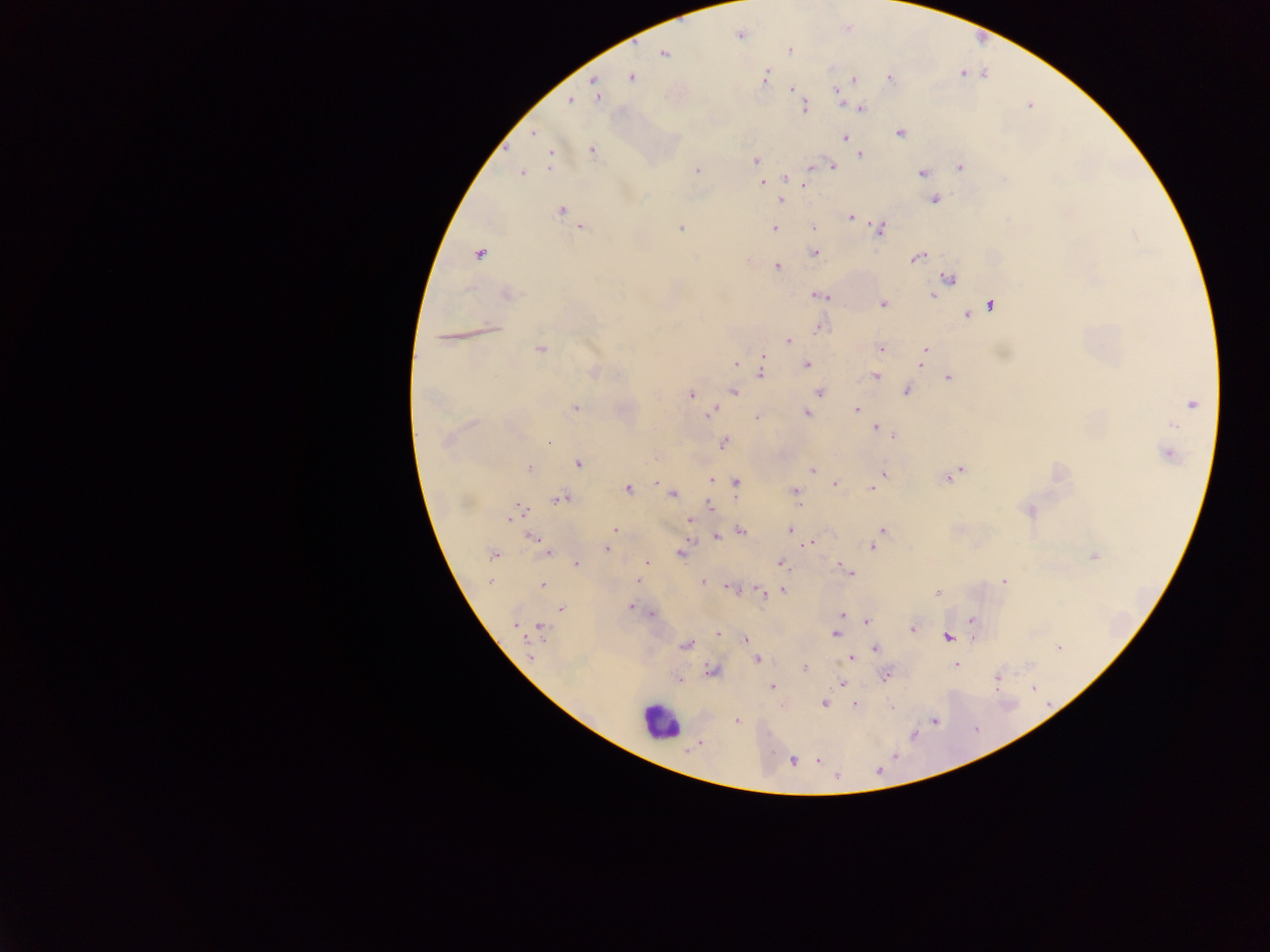
Approximate centers as (x, y) in pixels.
Summary:
  - Leukocyte locations: (658, 722)
  - Plasmodium parasite locations: (741, 35), (789, 50), (664, 53), (631, 77), (765, 77), (890, 78), (854, 80), (594, 81), (792, 89), (837, 92), (597, 95), (569, 101), (804, 107), (860, 108), (534, 133), (901, 133), (844, 137), (592, 150), (861, 155), (550, 158), (755, 160), (831, 166), (960, 167), (697, 170), (522, 172), (922, 173), (785, 178), (762, 183), (806, 185), (781, 200), (934, 200), (561, 211), (850, 216), (813, 227), (581, 228), (680, 228), (774, 229), (879, 229), (815, 253), (479, 254), (918, 257), (777, 267), (949, 278), (937, 287), (507, 294), (933, 294), (820, 295), (883, 304), (990, 305), (967, 315), (820, 327), (444, 338), (787, 341), (541, 349), (881, 349), (925, 350), (923, 356), (763, 359), (736, 363), (921, 364), (807, 365), (760, 371), (593, 372), (876, 375), (949, 378), (735, 391), (906, 391), (820, 392), (691, 394), (1192, 404), (575, 408), (856, 410), (711, 412), (807, 413), (757, 417), (1171, 424), (877, 428), (891, 435), (446, 441), (549, 442), (723, 443), (1168, 454), (578, 464), (529, 468), (812, 469), (960, 471), (884, 475), (948, 478), (711, 480), (659, 483), (736, 483), (834, 484), (628, 489), (872, 489), (795, 491), (672, 494), (561, 499), (797, 504), (711, 506), (519, 510), (1029, 511), (689, 520), (615, 529), (790, 530), (884, 530), (741, 531), (718, 537), (534, 539), (809, 543), (872, 547), (542, 548), (606, 548), (548, 552), (681, 552), (492, 555), (1093, 557), (647, 562), (577, 563), (781, 563), (847, 571), (637, 580), (490, 581), (703, 581), (1003, 581), (543, 585), (730, 588), (782, 590), (761, 591), (938, 593), (630, 607), (560, 609), (651, 614), (843, 615), (972, 619), (868, 621), (516, 625), (540, 627), (913, 629), (718, 633), (835, 634), (947, 638), (745, 639), (686, 644), (875, 648), (1059, 648), (530, 657), (850, 658), (758, 660), (955, 665), (804, 667), (712, 671), (885, 676), (997, 677), (679, 681), (844, 681), (772, 687), (1033, 689), (824, 703), (856, 705), (892, 707), (737, 720), (934, 721), (818, 760), (793, 761), (879, 770), (837, 777)
  - Field of view: single
  - Capture: mobile-phone photograph through a microscope
  - Image size: 1270×952 pixels
  - Preparation: thick blood film
  - Country: Ghana